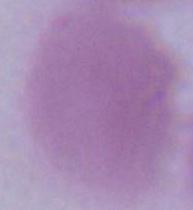
Summary:
  - Identification: erythrocyte
  - Modality: photomicrograph
  - Magnification: 1000x